Describe the morphology of the erythrocytes.
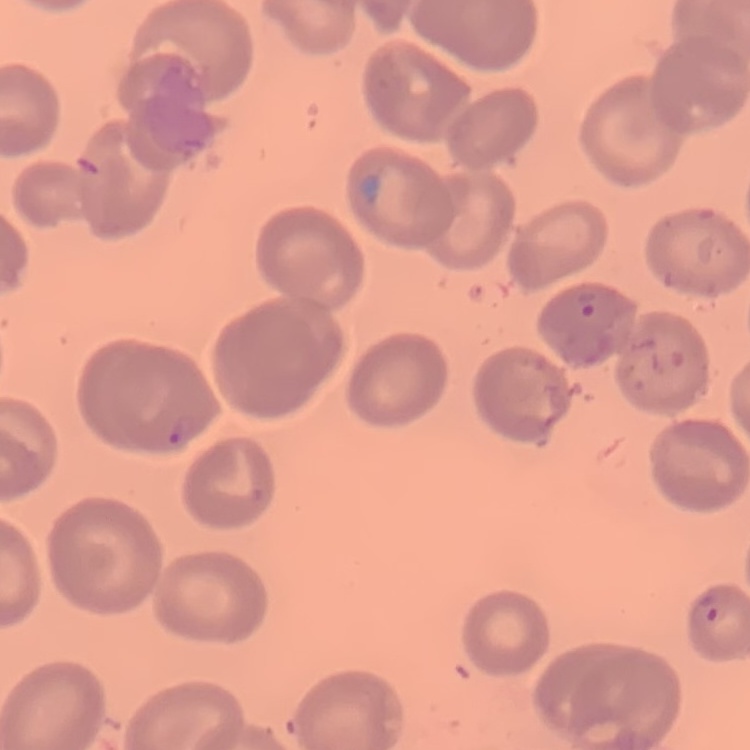
They show no rouleaux formation.

Thin peripheral smear. Stained with either Field's or Giemsa. One tile cut from a larger photomicrograph.